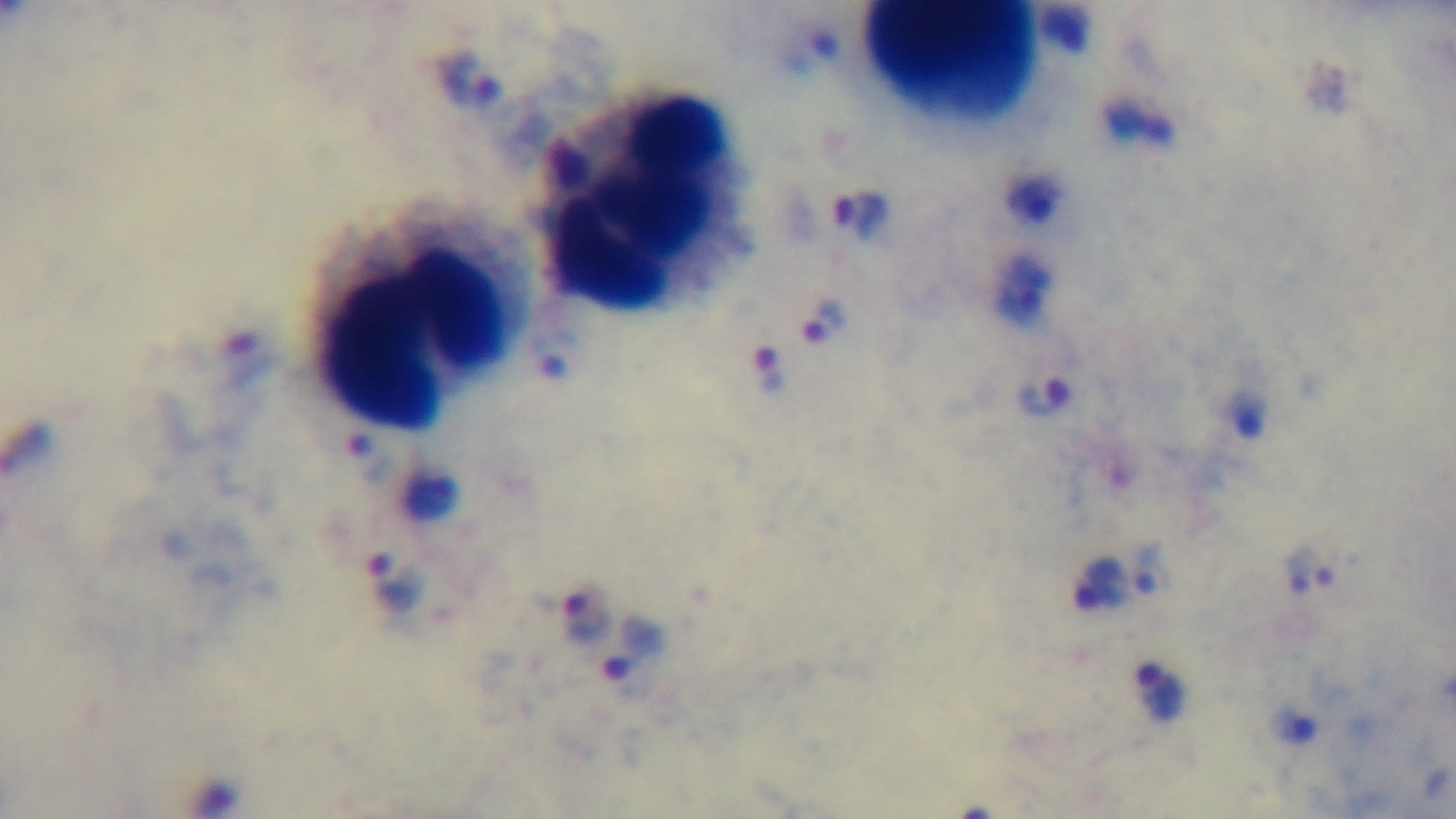
modality = light microscopy
objective = 100x oil immersion
field of view = single
malaria status = infected
preparation = thick
stain = Giemsa
capture = mounted 4K digital camera